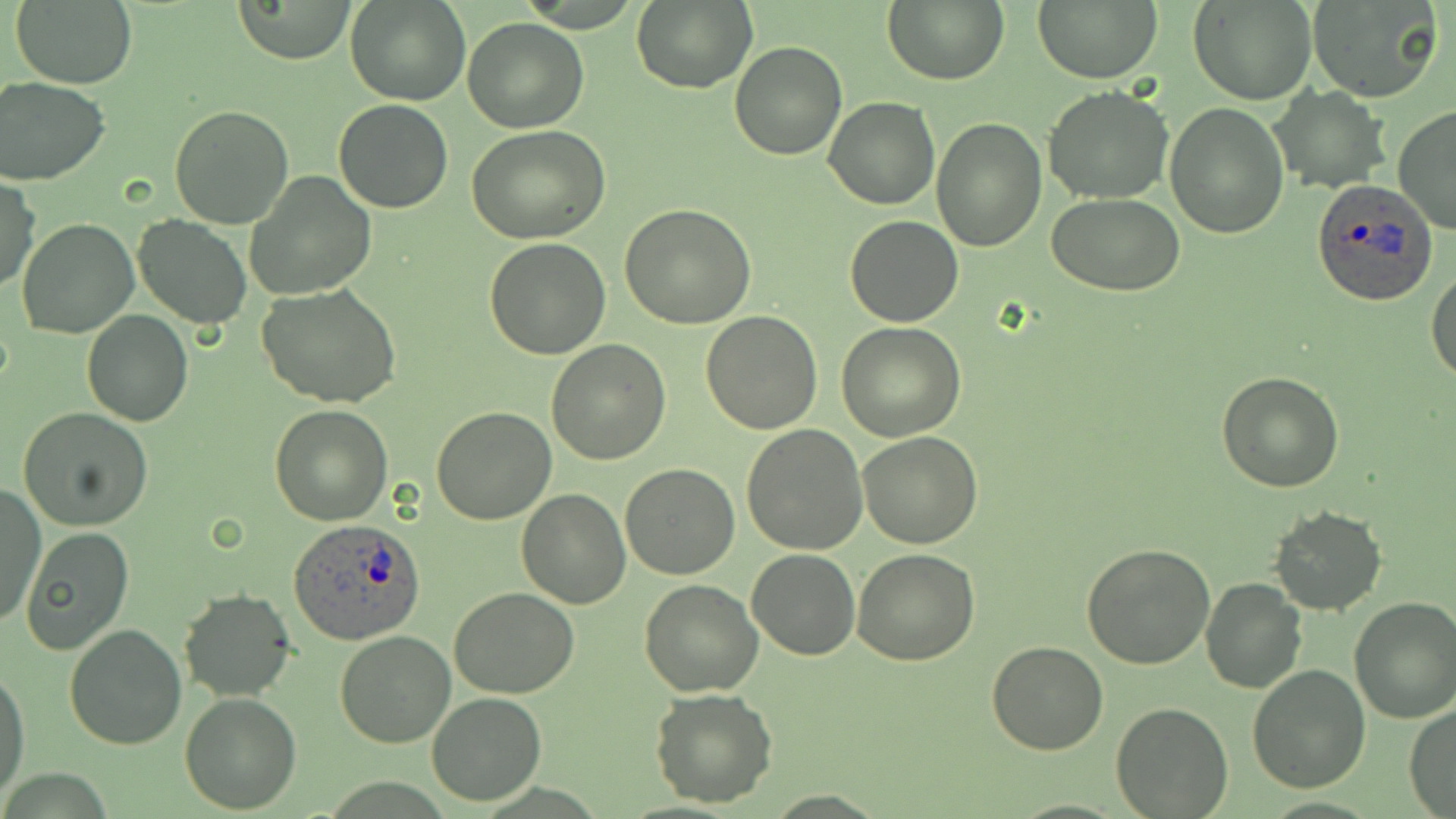
Approximate bounding boxes as named x1/y1/x2/y2 corners in pixels. Plasmodium ovale-infected red blood cell locations: (x1=1311, y1=180, x2=1438, y2=305), (x1=289, y1=518, x2=425, y2=645). Uninfected red blood cell locations: (x1=230, y1=0, x2=358, y2=64), (x1=347, y1=0, x2=470, y2=105), (x1=882, y1=0, x2=1008, y2=86), (x1=1033, y1=0, x2=1161, y2=82), (x1=1188, y1=0, x2=1315, y2=105), (x1=1306, y1=0, x2=1441, y2=103), (x1=631, y1=1, x2=756, y2=93), (x1=11, y1=2, x2=140, y2=88), (x1=462, y1=18, x2=588, y2=132), (x1=729, y1=40, x2=846, y2=161), (x1=0, y1=75, x2=113, y2=186), (x1=1269, y1=86, x2=1391, y2=194), (x1=1044, y1=87, x2=1174, y2=204), (x1=824, y1=96, x2=940, y2=210), (x1=333, y1=100, x2=453, y2=213), (x1=1165, y1=101, x2=1289, y2=239), (x1=169, y1=103, x2=293, y2=230), (x1=1392, y1=104, x2=1456, y2=232), (x1=932, y1=116, x2=1046, y2=252), (x1=466, y1=127, x2=611, y2=243), (x1=245, y1=169, x2=376, y2=299), (x1=1, y1=177, x2=40, y2=293), (x1=1048, y1=193, x2=1186, y2=295), (x1=620, y1=204, x2=756, y2=329), (x1=132, y1=215, x2=252, y2=328), (x1=845, y1=215, x2=963, y2=327), (x1=17, y1=218, x2=139, y2=339), (x1=483, y1=237, x2=611, y2=359), (x1=1427, y1=267, x2=1456, y2=383), (x1=257, y1=285, x2=401, y2=409), (x1=81, y1=310, x2=193, y2=427), (x1=700, y1=310, x2=824, y2=434), (x1=837, y1=321, x2=966, y2=442), (x1=545, y1=338, x2=672, y2=465), (x1=1216, y1=372, x2=1344, y2=492), (x1=269, y1=405, x2=392, y2=525), (x1=431, y1=406, x2=556, y2=525), (x1=19, y1=408, x2=155, y2=530), (x1=741, y1=424, x2=869, y2=555), (x1=856, y1=431, x2=982, y2=549), (x1=621, y1=464, x2=740, y2=581), (x1=515, y1=478, x2=739, y2=595), (x1=0, y1=485, x2=46, y2=632), (x1=515, y1=488, x2=632, y2=610), (x1=1269, y1=506, x2=1389, y2=616), (x1=21, y1=528, x2=133, y2=655), (x1=1082, y1=542, x2=1215, y2=668), (x1=852, y1=547, x2=980, y2=664), (x1=747, y1=548, x2=860, y2=660), (x1=639, y1=579, x2=762, y2=698), (x1=1201, y1=579, x2=1307, y2=693), (x1=450, y1=586, x2=580, y2=697), (x1=179, y1=589, x2=295, y2=701), (x1=1348, y1=598, x2=1456, y2=723), (x1=64, y1=623, x2=188, y2=750), (x1=333, y1=630, x2=456, y2=748), (x1=987, y1=639, x2=1108, y2=755), (x1=0, y1=664, x2=30, y2=799), (x1=1246, y1=664, x2=1371, y2=793), (x1=650, y1=687, x2=779, y2=808), (x1=180, y1=691, x2=301, y2=814), (x1=427, y1=691, x2=546, y2=806), (x1=1113, y1=703, x2=1232, y2=818), (x1=1404, y1=703, x2=1456, y2=816). Slide-level diagnosis: Plasmodium ovale. Captured at 1000x magnification. Light microscopy. Image is 1456×819 pixels. Thin blood smear. Single field of view. May-Grünwald-Giemsa-stained preparation.